Report the malaria status of this cell.
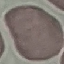
Uninfected.

Summary:
  - Stain: Giemsa
  - Preparation: thin blood smear
  - Image type: automatically extracted cell patch, resized to 64 × 64 pixels
  - Capture: smartphone camera at the microscope eyepiece